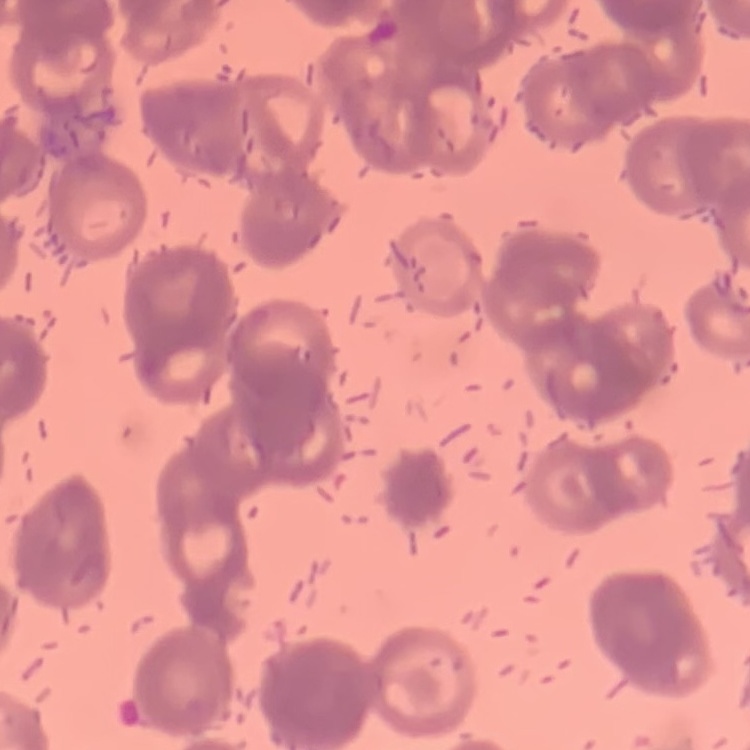

red blood cell morphology = rouleaux formation
preparation = thin peripheral smear
stain = Field's or Giemsa
image type = square crop of a larger photomicrograph